State which cell type is depicted.
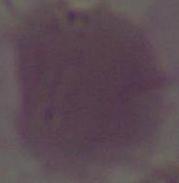

This is an erythrocyte.

Micrograph. 1000x magnification.